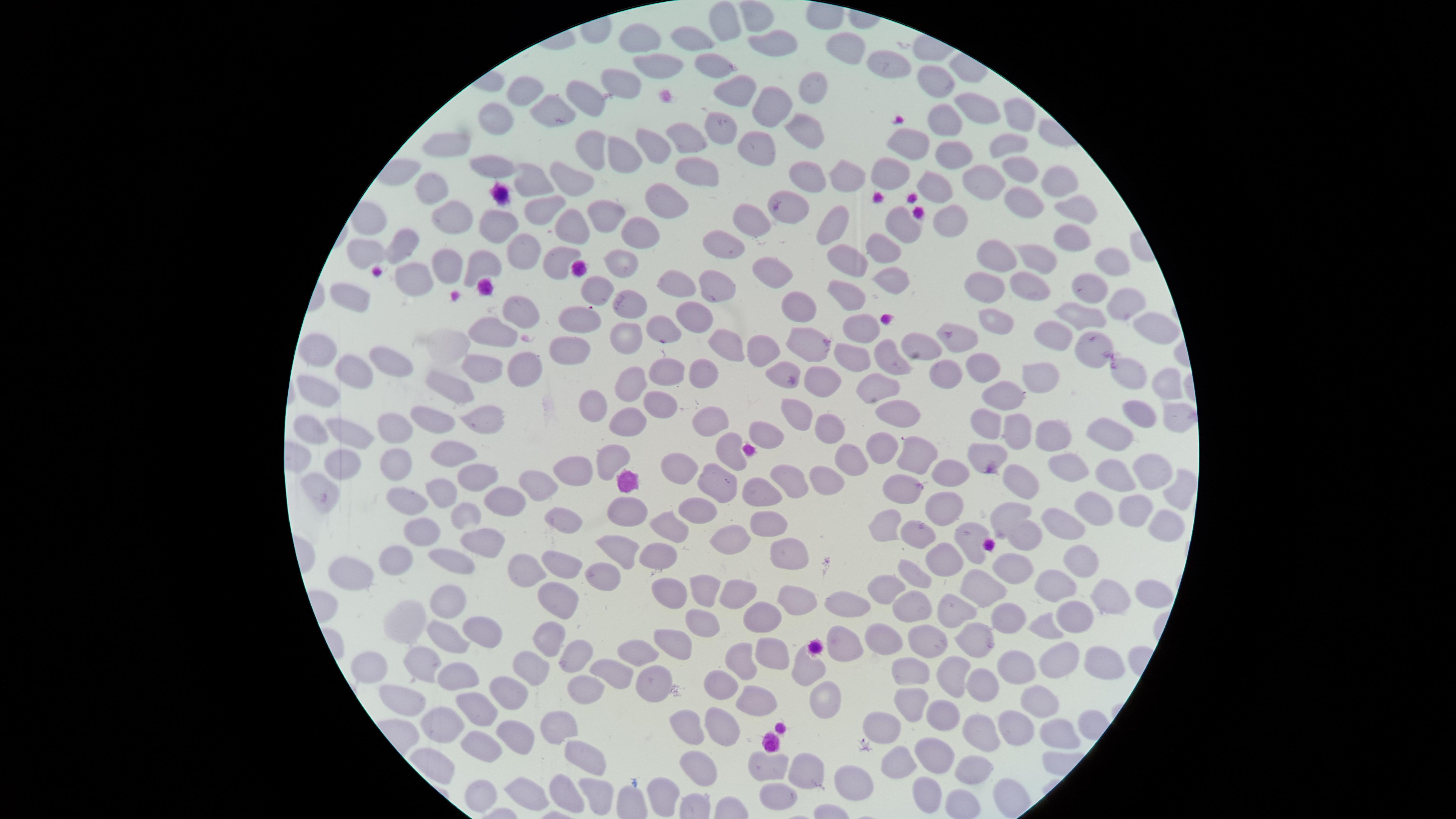
Approximate marker points as (x, y) in pixels. Uninfected RBCs: (755, 15), (725, 24), (635, 34), (690, 37), (766, 44), (851, 52), (709, 64), (652, 67), (885, 72), (939, 77), (617, 85), (732, 91), (814, 91), (526, 92), (592, 99), (765, 106), (557, 112), (976, 114), (502, 115), (939, 115), (1017, 121), (722, 123), (809, 129), (686, 136), (696, 139), (1008, 143), (651, 144), (913, 146), (451, 147), (586, 148), (761, 151), (947, 154), (620, 155), (1014, 165), (695, 167), (486, 168), (894, 172), (852, 179), (817, 181), (566, 183), (532, 184), (990, 184), (1054, 184), (428, 185), (941, 188), (663, 195), (1019, 201), (793, 206), (539, 209), (1078, 211), (940, 219), (453, 220), (610, 220), (749, 220), (901, 223), (562, 224), (502, 227), (833, 227), (631, 238), (1069, 238), (403, 240), (718, 245), (884, 245), (521, 248), (843, 254), (363, 257), (997, 257), (1033, 258), (558, 260), (1108, 261), (483, 262), (622, 264), (446, 268), (768, 268), (890, 279), (419, 281), (987, 284), (1022, 284), (672, 285), (1081, 287), (843, 290), (596, 291), (720, 296), (624, 301), (1117, 301), (350, 302), (801, 307), (519, 313), (690, 316), (580, 319), (1091, 322), (997, 324), (855, 327), (660, 331), (497, 332), (1050, 335), (1163, 335), (622, 338), (957, 340), (722, 344), (807, 344), (1092, 344), (576, 348), (318, 351), (758, 352), (922, 352), (852, 357), (391, 361), (890, 363), (481, 367), (525, 369), (981, 370), (671, 373), (779, 373), (1125, 373), (1041, 376), (699, 377), (943, 378), (355, 379), (1163, 382), (828, 383), (881, 384), (631, 387), (457, 391), (1002, 391), (323, 393), (596, 401), (661, 402), (801, 415), (900, 416), (1138, 417), (1170, 417), (435, 419), (707, 422), (483, 424), (627, 424), (388, 425), (991, 425), (824, 426), (1021, 430), (1048, 430), (312, 433), (345, 433), (766, 436), (1115, 437), (886, 449), (453, 450), (729, 452), (982, 456), (848, 458), (605, 459), (394, 462), (923, 462), (1074, 464), (342, 467), (683, 467), (579, 472), (1151, 473), (951, 474), (475, 476), (822, 479), (718, 480), (1112, 480), (793, 482), (537, 486), (765, 489), (1021, 489), (1181, 491), (324, 492), (908, 492), (437, 493), (407, 499), (509, 499), (701, 507), (1088, 508), (947, 510), (1129, 510), (468, 515), (624, 515), (1003, 518), (561, 520), (883, 523), (669, 525), (1164, 525), (760, 526), (1067, 530), (432, 533), (918, 534), (972, 536), (1030, 536), (737, 540), (481, 542), (622, 546), (783, 552), (653, 553), (949, 556), (453, 559), (557, 560), (1077, 560), (401, 565), (1013, 566), (531, 571), (916, 576), (355, 578), (598, 578), (888, 586), (1056, 586), (974, 589), (667, 591), (705, 591), (735, 591), (794, 595), (1111, 596), (1150, 596), (557, 599), (953, 603), (445, 604), (844, 606), (911, 609), (1075, 615), (764, 616), (1008, 618), (701, 621), (417, 623), (1044, 628), (484, 631), (552, 636), (879, 638), (450, 639), (976, 639), (927, 640), (669, 641), (847, 644), (773, 652), (642, 655), (425, 656), (1106, 656), (580, 657), (744, 663), (534, 665), (1059, 665), (805, 667), (1020, 669), (956, 670), (375, 671), (908, 673), (462, 674), (614, 677), (655, 680), (981, 682), (722, 684), (507, 694), (589, 694), (1036, 699), (759, 701), (408, 703), (481, 705), (827, 706), (909, 706), (943, 718), (439, 723), (884, 723), (686, 728), (513, 729), (556, 729), (719, 730), (1056, 735), (977, 737), (1012, 737), (481, 748), (929, 752), (589, 759), (897, 766), (769, 768), (799, 770), (696, 771), (974, 771), (851, 782), (477, 790), (565, 790), (926, 790), (599, 793), (656, 793), (527, 795), (782, 795). Image is 1456×819 pixels. Thin blood smear. Photographed with a smartphone camera through the microscope eyepiece. Presence: no malaria parasites identified. The visible region is circular. Giemsa stain. Single field of view.